Outline each blood parasite and name the species.
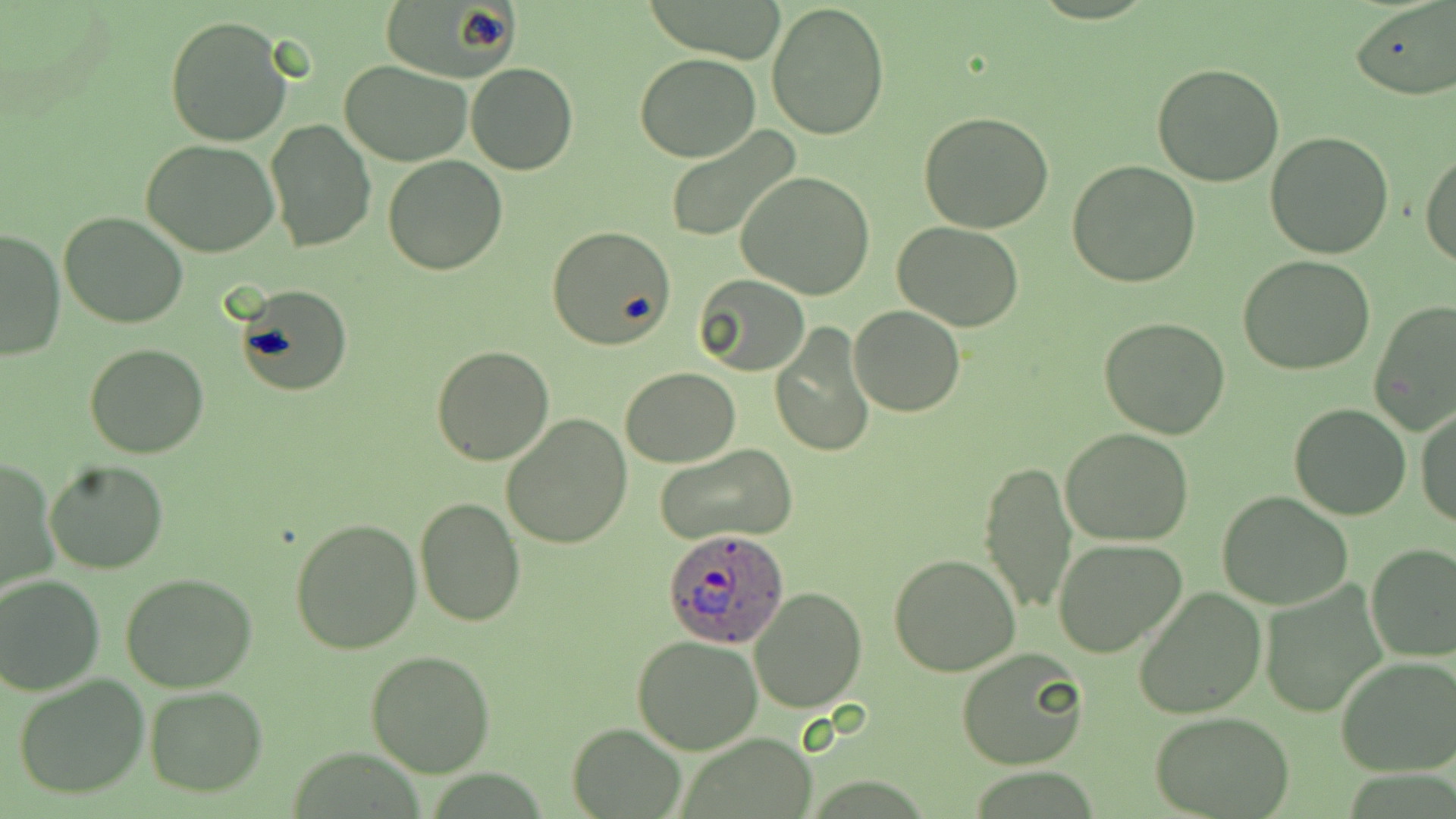

Approximate bounding boxes as [x1, y1, x2, y2] in pixels.
Plasmodium ovale-infected red blood cells: [661, 526, 792, 647].
No Plasmodium falciparum, Plasmodium malariae, Plasmodium vivax, Babesia divergens, or Trypanosoma brucei observed.

Uninfected red blood cell locations: [379, 0, 519, 82], [654, 0, 780, 65], [766, 1, 890, 139], [1351, 3, 1454, 100], [164, 14, 294, 147], [637, 53, 758, 161], [338, 60, 473, 165], [465, 62, 578, 176], [1152, 62, 1285, 187], [918, 110, 1055, 233], [265, 118, 377, 253], [666, 126, 800, 244], [1265, 130, 1396, 260], [142, 138, 279, 258], [1421, 146, 1455, 267], [383, 156, 507, 275], [1067, 159, 1201, 287], [738, 172, 876, 300], [59, 210, 187, 329], [893, 221, 1024, 331], [545, 225, 677, 350], [0, 228, 65, 359], [1237, 255, 1377, 376], [694, 274, 810, 377], [236, 286, 351, 395], [1370, 300, 1456, 435], [849, 304, 964, 417], [1099, 316, 1232, 440], [769, 324, 876, 457], [84, 344, 210, 459], [430, 344, 556, 465], [621, 366, 741, 468], [1287, 402, 1412, 521], [1415, 404, 1456, 528], [501, 415, 633, 550], [1060, 428, 1195, 547], [654, 442, 798, 545], [2, 458, 58, 598], [980, 459, 1078, 616], [42, 460, 169, 573], [1216, 490, 1352, 610], [414, 495, 525, 627], [289, 517, 422, 653], [1051, 538, 1188, 658], [1365, 543, 1456, 662], [889, 553, 1021, 677], [118, 572, 262, 694], [0, 574, 106, 694], [1260, 581, 1389, 716], [1133, 585, 1266, 719], [750, 587, 866, 714], [633, 636, 764, 754], [956, 647, 1091, 771], [365, 648, 495, 776], [1336, 653, 1456, 776], [11, 673, 152, 800], [144, 686, 267, 796], [1152, 712, 1295, 817], [567, 723, 685, 817]. Slide-level diagnosis: Plasmodium ovale. May-Grünwald-Giemsa stain. Image is 1456×819 pixels. Single field of view. Light microscopy. Captured at 1000x magnification. Thin blood film.